Outline each blood parasite and name the species.
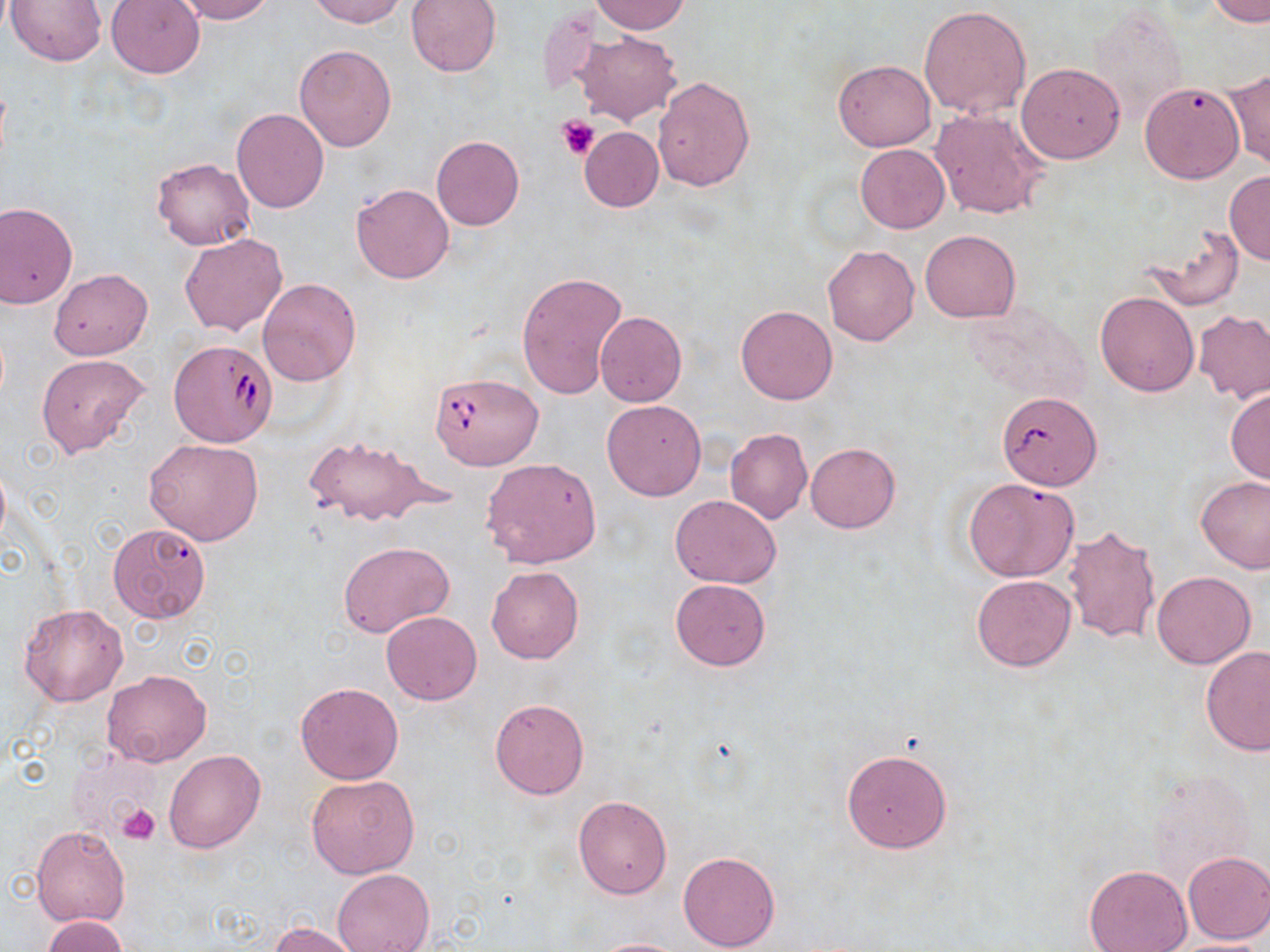
Approximate bounding boxes as (x1, y1, x2, y2) in pixels.
Babesia divergens-infected red blood cells: (167, 338, 276, 448), (430, 372, 543, 471).
No Plasmodium falciparum, Plasmodium ovale, Plasmodium malariae, Plasmodium vivax, or Trypanosoma brucei observed.

Platelet locations: (555, 114, 598, 159), (115, 802, 161, 845). Uninfected red blood cell locations: (5, 0, 109, 67), (106, 0, 205, 78), (176, 0, 274, 23), (307, 0, 408, 27), (406, 0, 502, 77), (1208, 0, 1270, 25), (588, 1, 690, 35), (919, 6, 1031, 119), (537, 7, 606, 99), (1087, 7, 1188, 123), (575, 31, 681, 125), (293, 44, 397, 152), (833, 60, 936, 151), (1017, 63, 1125, 163), (1225, 68, 1269, 169), (653, 76, 755, 191), (1140, 82, 1246, 184), (931, 107, 1049, 220), (231, 108, 330, 214), (580, 127, 664, 212), (432, 137, 525, 231), (855, 145, 949, 232), (150, 156, 256, 249), (1223, 170, 1270, 265), (351, 182, 453, 284), (0, 203, 78, 307), (1144, 224, 1245, 311), (920, 230, 1021, 322), (179, 234, 287, 336), (822, 245, 919, 346), (49, 268, 153, 360), (516, 270, 627, 400), (258, 278, 361, 385), (1094, 292, 1199, 397), (736, 303, 838, 405), (960, 304, 1091, 408), (1194, 310, 1270, 404), (595, 311, 686, 407), (36, 353, 150, 459), (1226, 386, 1270, 484), (995, 393, 1101, 493), (602, 399, 707, 500), (724, 428, 812, 525), (303, 434, 442, 529), (144, 438, 264, 545), (806, 443, 899, 532), (480, 458, 602, 568), (1196, 474, 1270, 574), (963, 477, 1079, 582), (670, 495, 781, 588), (106, 522, 213, 626), (1064, 524, 1161, 645), (339, 541, 454, 637), (487, 565, 584, 663), (1151, 571, 1255, 668), (972, 575, 1076, 670), (670, 578, 771, 670), (18, 604, 129, 706), (381, 611, 482, 705), (1201, 646, 1269, 757), (102, 669, 211, 766), (295, 681, 405, 785), (490, 699, 589, 799), (841, 747, 953, 853), (164, 748, 266, 853), (306, 773, 420, 878), (573, 796, 672, 899), (31, 825, 130, 927), (1182, 851, 1270, 945), (677, 852, 780, 951), (1083, 865, 1194, 952), (332, 868, 434, 952), (41, 915, 129, 951), (268, 922, 366, 952), (588, 937, 690, 952), (1161, 937, 1270, 951). Slide-level diagnosis: Babesia divergens. Light microscopy. Captured at 1000x magnification. May-Grünwald-Giemsa stain. Thin blood smear. One field of a larger specimen. Image is 1270×952 pixels.